Assess this cell for malaria.
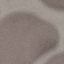
Uninfected.

Summary:
  - Preparation: thin blood film
  - Capture: smartphone camera at the microscope eyepiece
  - Image type: cell patch, automatically extracted from a larger field of view and resized to 64 × 64 pixels
  - Stain: Giemsa